Identify the blood parasite species.
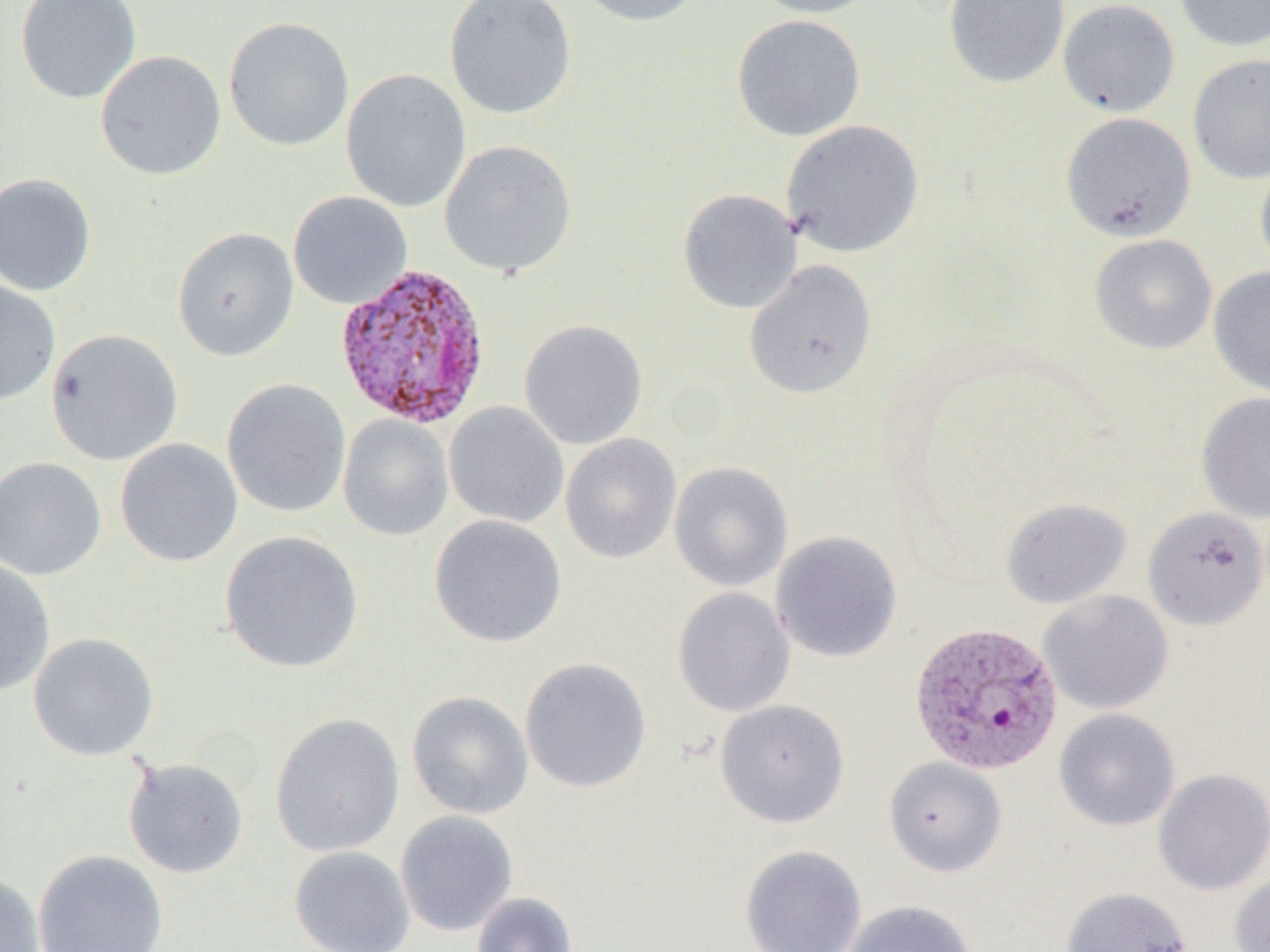
Plasmodium vivax.

Summary:
  - Coordinate format: approximate bounding boxes as [x1, y1, x2, y2] in pixels
  - Plasmodium vivax-infected red blood cell locations: [323, 265, 480, 431], [914, 623, 1070, 778]
  - Uninfected red blood cell locations: [15, 0, 142, 104], [444, 0, 578, 120], [573, 0, 705, 27], [747, 0, 884, 18], [943, 0, 1070, 89], [1057, 0, 1181, 117], [1174, 0, 1270, 52], [731, 14, 866, 142], [223, 17, 356, 152], [94, 50, 227, 181], [1187, 52, 1270, 184], [341, 69, 472, 214], [1060, 111, 1196, 242], [781, 119, 924, 257], [439, 140, 577, 278], [1254, 159, 1270, 280], [0, 172, 97, 297], [678, 188, 802, 314], [288, 191, 413, 310], [172, 227, 299, 362], [1089, 234, 1218, 355], [744, 260, 878, 399], [1208, 267, 1270, 398], [0, 279, 61, 406], [519, 319, 648, 450], [45, 329, 184, 466], [222, 379, 351, 518], [1196, 392, 1270, 523], [444, 402, 569, 528], [338, 415, 454, 541], [560, 433, 682, 564], [115, 438, 243, 567], [0, 457, 107, 581], [669, 462, 794, 591], [1001, 498, 1132, 609], [1142, 506, 1268, 630], [428, 515, 567, 648], [219, 530, 364, 674], [771, 531, 903, 663], [0, 558, 57, 696], [672, 587, 795, 717], [1037, 590, 1174, 714], [28, 632, 160, 761], [519, 657, 652, 793], [407, 691, 534, 819], [715, 699, 850, 828], [1053, 708, 1181, 831], [269, 713, 405, 857], [122, 757, 249, 879], [884, 757, 1007, 877], [1153, 767, 1270, 895], [394, 811, 518, 936], [739, 845, 867, 952], [288, 846, 416, 952], [32, 848, 169, 952], [0, 872, 45, 952], [1229, 872, 1270, 952], [1060, 885, 1193, 952], [471, 892, 579, 952], [843, 901, 978, 952]
  - Magnification: 1000x
  - Field of view: one of a larger specimen
  - Preparation: thin blood smear
  - Image size: 1270×952 pixels
  - Modality: optical microscopy